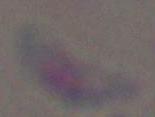
magnification = 1000x
identification = Toxoplasma gondii
modality = micrograph